Describe the morphology of the red blood cells.
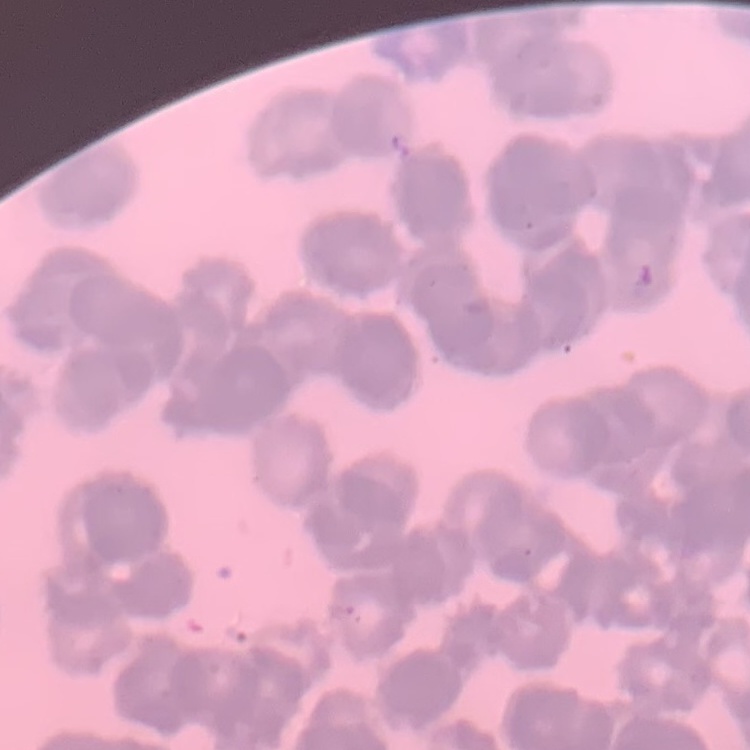

They show rouleaux formation.

Field's or Giemsa stain. One tile cut from a larger photomicrograph. Thin blood smear.